Locate every Plasmodium parasite and every leukocyte.
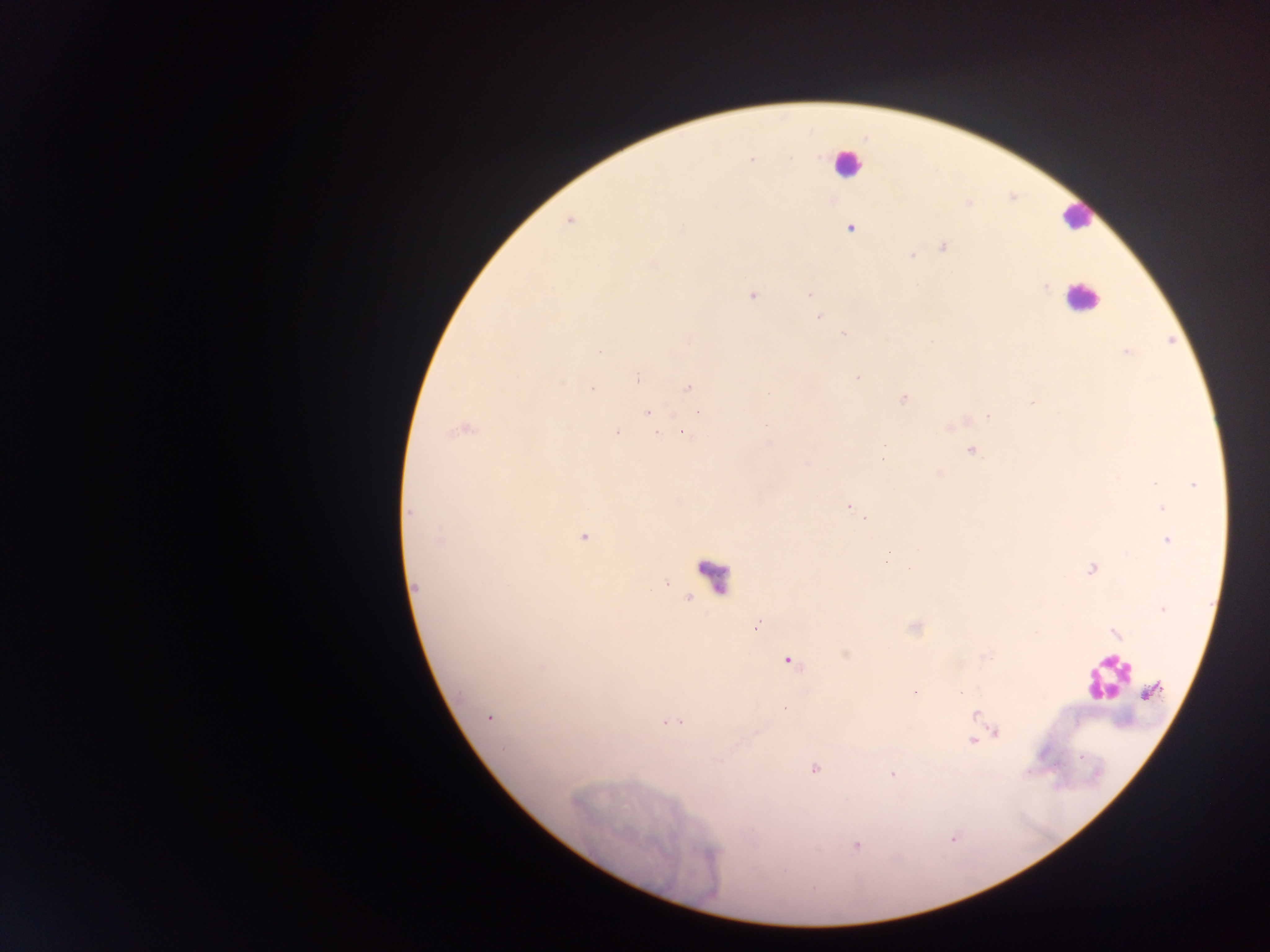
Approximate centers as {x, y} in pixels.
Plasmodium parasites: {752, 160}, {568, 221}, {850, 228}, {682, 230}, {943, 247}, {911, 255}, {653, 264}, {1045, 287}, {810, 294}, {752, 296}, {818, 317}, {843, 334}, {599, 351}, {1126, 352}, {636, 378}, {857, 378}, {689, 387}, {592, 388}, {769, 394}, {903, 399}, {647, 412}, {988, 416}, {766, 425}, {463, 430}, {617, 433}, {657, 433}, {683, 433}, {884, 446}, {971, 451}, {883, 458}, {808, 464}, {1155, 484}, {1194, 484}, {848, 507}, {1162, 508}, {410, 512}, {864, 518}, {584, 537}, {440, 539}, {1168, 540}, {888, 553}, {909, 569}, {1091, 569}, {416, 586}, {1162, 608}, {757, 625}, {789, 662}, {961, 692}, {976, 714}, {490, 717}, {668, 722}, {679, 722}, {997, 732}, {972, 740}, {814, 769}, {892, 775}, {856, 845}.
Leukocytes: {846, 163}, {1076, 217}, {1082, 297}, {712, 577}, {1108, 677}.

Summary:
  - Capture: mobile-phone photograph through a microscope
  - Preparation: thick blood film
  - Image size: 1270×952 pixels
  - Country: Ghana
  - Field of view: single